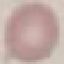
malaria status = uninfected
preparation = thin blood smear
image type = cell patch, automatically extracted from a larger field of view and resized to 64 × 64 pixels
stain = Giemsa
capture = smartphone through the microscope eyepiece